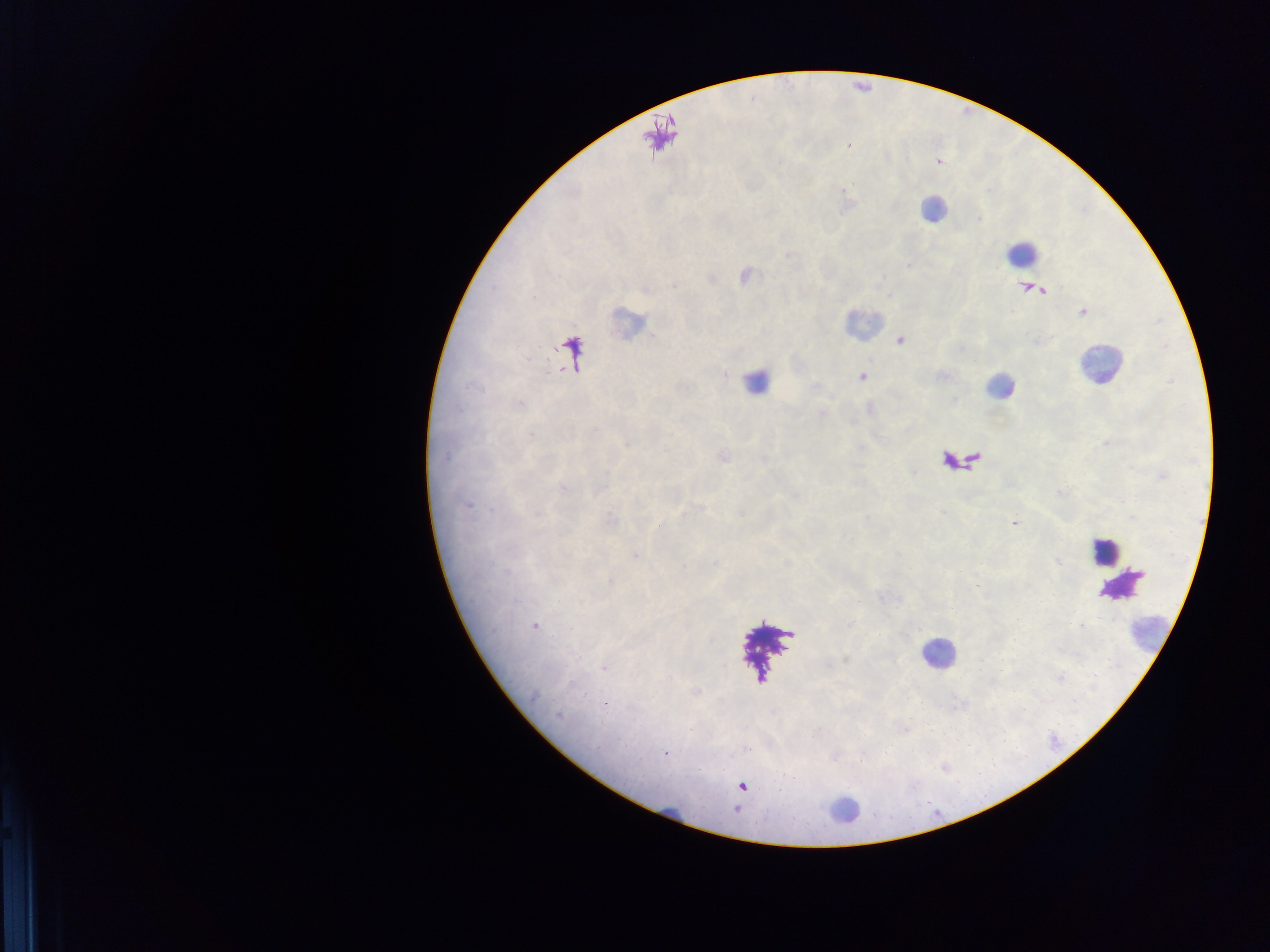

{
  "malaria_parasite_locations": "approximate centers as [x, y] in pixels: [848, 146], [938, 162], [845, 192], [980, 217], [908, 264], [1013, 521], [605, 704], [666, 754]",
  "capture": "mobile-phone photograph through a microscope",
  "field_of_view": "single",
  "preparation": "thick blood film",
  "image_size": "1270×952 pixels",
  "country": "Ghana",
  "leukocyte_locations": "approximate centers as [x, y] in pixels: [863, 323], [1093, 361], [760, 385], [995, 389], [938, 652], [845, 804]"
}